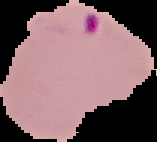
preparation = thin blood smear
image type = segmented cell region with the area outside set to black
image size = 157×142 pixels
result = malaria parasites detected